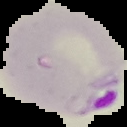
preparation: thin blood film
result: malaria parasites detected
image_type: segmented cell region on a black background
image_size: 127×127 pixels